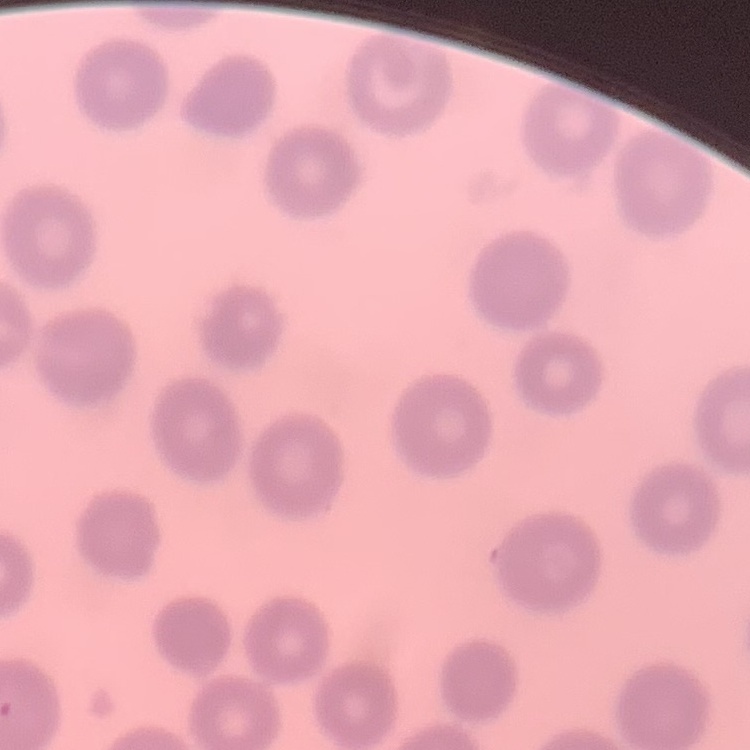
erythrocyte morphology = no rouleaux formation
image type = one tile cut from a larger photomicrograph
stain = Field's or Giemsa
preparation = thin blood smear